Assess this cell for malaria.
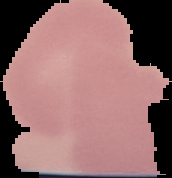

Uninfected.

Image is 172×178 pixels. From a thin blood smear. Segmented cell region on a black background.